Assess this cell for malaria.
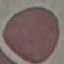

Uninfected.

Giemsa-stained preparation. Thin blood smear. Automatically extracted cell patch, resized to 64 × 64 pixels. Photographed with a smartphone camera at the microscope eyepiece.